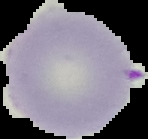

Malaria status: uninfected. From a thin blood film. The area outside the segmented cell region is set to black. Image is 148×139 pixels.